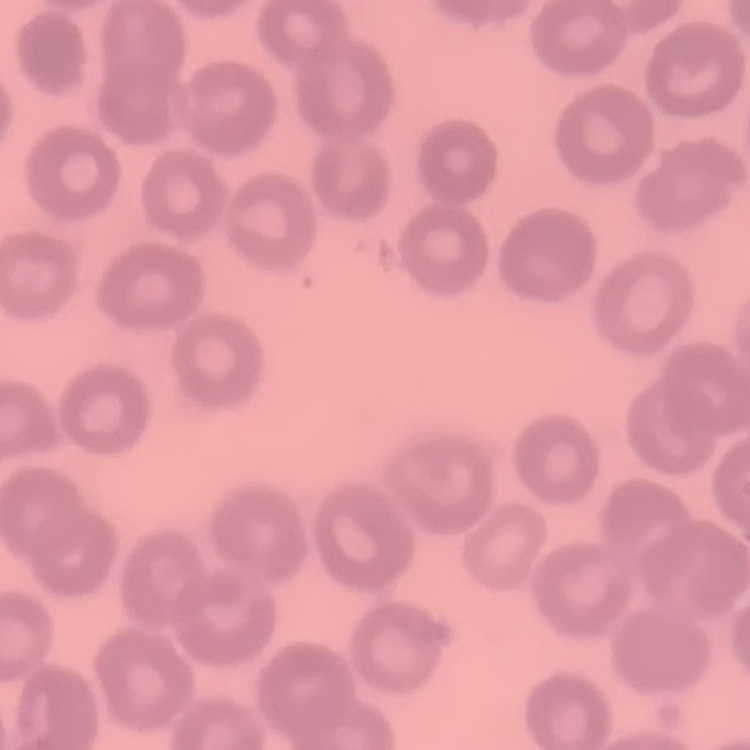
The erythrocytes show no rouleaux formation. Stained with either Field's or Giemsa. Thin blood film. One tile cut from a larger photomicrograph.